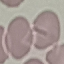

Summary:
  - Malaria status: uninfected
  - Stain: Giemsa
  - Image type: automatically extracted cell patch, resized to 64 × 64 pixels
  - Preparation: thin blood smear
  - Capture: smartphone camera at the microscope eyepiece